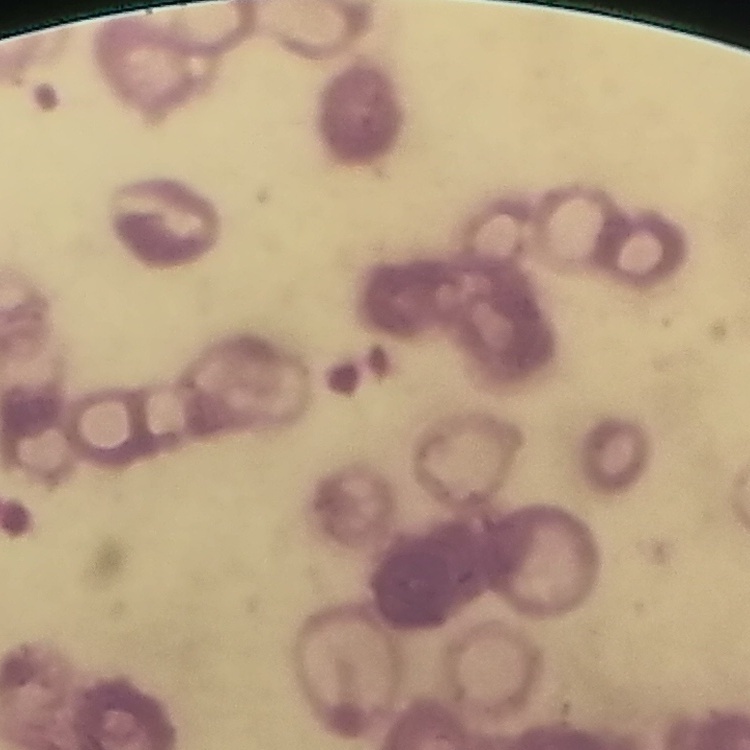
erythrocyte_morphology: rouleaux formation
stain: Field's or Giemsa
preparation: thin blood film
image_type: one tile cut from a larger photomicrograph